Name the parasite shown.
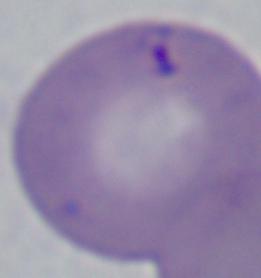

This is Babesia.

Summary:
  - Modality: micrograph
  - Magnification: 1000x